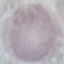
Summary:
  - Malaria status: uninfected
  - Preparation: thin blood smear
  - Stain: Giemsa
  - Capture: smartphone camera at the microscope eyepiece
  - Image type: cell patch, automatically extracted from a larger field of view and resized to 64 × 64 pixels